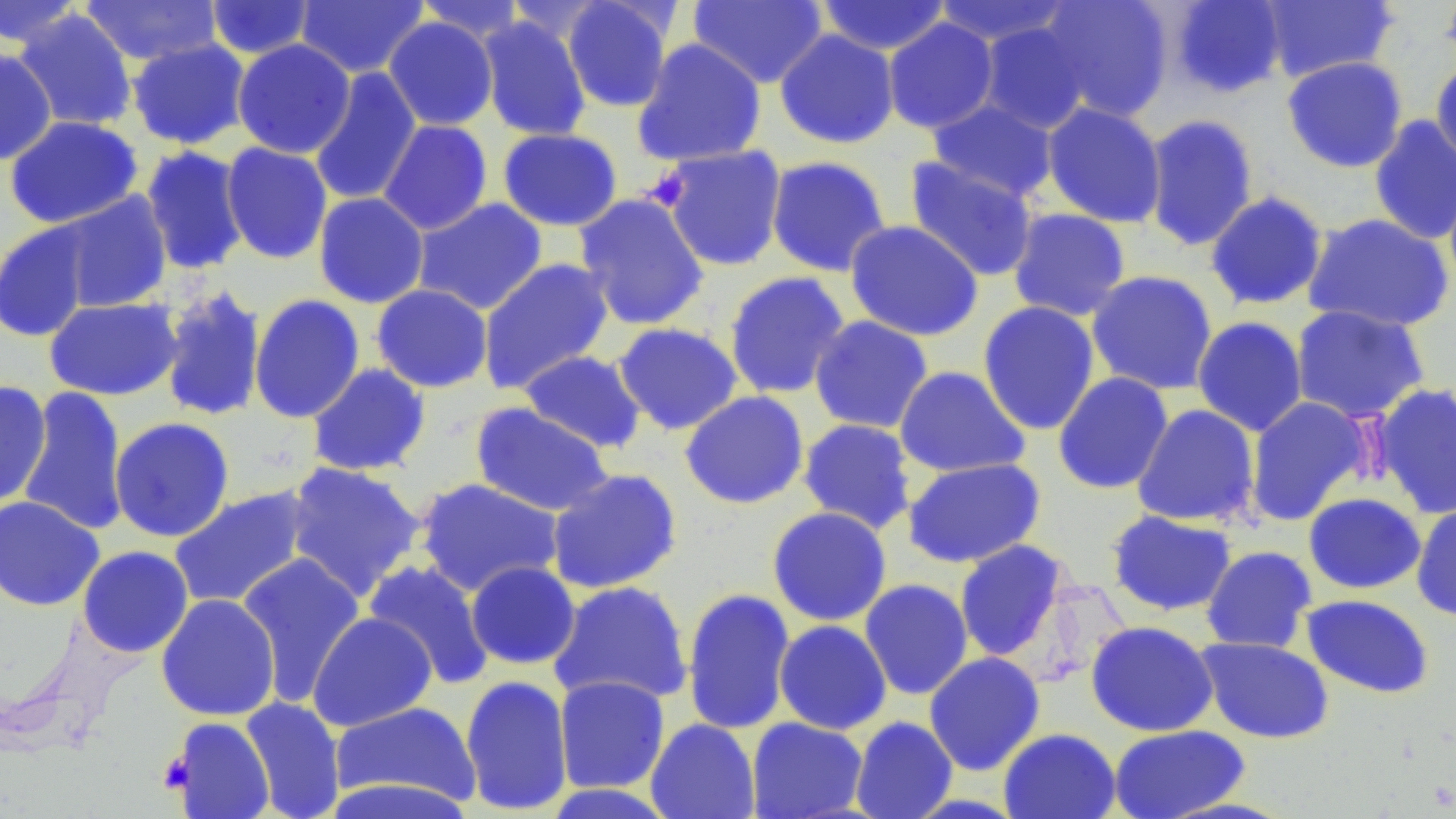

Summary:
  - Coordinate format: approximate bounding boxes as [x1, y1, x2, y2] in pixels
  - Platelet locations: [643, 167, 691, 211], [158, 751, 193, 794]
  - Uninfected red blood cell locations: [294, 0, 429, 78], [561, 0, 675, 113], [688, 0, 829, 88], [815, 0, 952, 56], [932, 0, 1074, 48], [1036, 0, 1174, 122], [1168, 0, 1287, 98], [1259, 0, 1399, 84], [1439, 0, 1456, 69], [0, 1, 85, 49], [79, 1, 223, 66], [205, 1, 316, 59], [412, 1, 529, 44], [13, 9, 138, 132], [477, 15, 592, 141], [383, 17, 499, 131], [882, 17, 999, 134], [976, 21, 1093, 134], [774, 28, 900, 149], [126, 38, 251, 150], [631, 38, 767, 167], [232, 39, 356, 158], [0, 48, 58, 165], [1430, 54, 1456, 169], [1282, 56, 1408, 173], [308, 67, 422, 206], [926, 98, 1059, 203], [1041, 101, 1167, 228], [1142, 113, 1259, 252], [1368, 115, 1456, 245], [4, 116, 144, 229], [378, 119, 493, 235], [497, 127, 623, 231], [221, 142, 333, 265], [139, 145, 250, 275], [657, 145, 788, 272], [765, 155, 892, 277], [904, 156, 1039, 282], [1205, 190, 1329, 311], [54, 191, 173, 313], [313, 192, 429, 308], [573, 193, 710, 331], [412, 197, 548, 316], [1007, 207, 1131, 322], [1302, 212, 1454, 332], [844, 219, 984, 341], [0, 221, 96, 343], [477, 257, 615, 394], [723, 270, 850, 400], [1086, 270, 1219, 396], [371, 284, 493, 393], [158, 285, 268, 423], [249, 294, 365, 423], [44, 297, 182, 401], [977, 301, 1101, 436], [1290, 304, 1430, 424], [809, 315, 934, 434], [1192, 315, 1308, 437], [611, 322, 743, 435], [518, 349, 648, 454], [306, 362, 431, 477], [894, 366, 1030, 478], [1052, 372, 1174, 494], [0, 380, 52, 509], [1371, 382, 1456, 520], [17, 386, 130, 537], [680, 390, 809, 509], [1245, 396, 1372, 525], [469, 403, 614, 517], [1131, 404, 1261, 528], [109, 417, 235, 542], [797, 418, 918, 534], [901, 457, 1047, 568], [283, 461, 425, 602], [546, 468, 683, 594], [414, 477, 565, 598], [168, 487, 313, 610], [1303, 492, 1427, 594], [0, 495, 104, 611], [1411, 502, 1456, 622], [767, 506, 892, 627], [1105, 510, 1238, 617], [953, 539, 1071, 662], [77, 545, 194, 657], [1201, 545, 1317, 653], [235, 552, 366, 706], [363, 559, 495, 690], [465, 561, 581, 670], [859, 578, 974, 700], [548, 581, 694, 706], [681, 587, 796, 736], [156, 593, 281, 721], [1301, 594, 1435, 699], [307, 612, 437, 732], [773, 620, 892, 735], [1085, 620, 1218, 737], [1196, 637, 1334, 744], [923, 652, 1045, 775], [459, 674, 574, 814], [553, 675, 670, 794], [239, 697, 346, 819], [329, 700, 481, 806], [167, 716, 275, 819], [849, 716, 958, 819], [746, 717, 869, 819], [645, 718, 760, 819], [1108, 724, 1251, 819], [998, 727, 1121, 819], [321, 777, 477, 819], [539, 783, 679, 818]
  - Slide-level diagnosis: no evidence of blood parasites
  - Modality: optical microscopy
  - Field of view: single
  - Preparation: thin blood smear
  - Stain: May-Grünwald-Giemsa
  - Magnification: 1000x
  - Image size: 1456×819 pixels